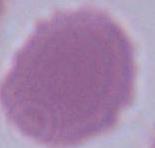
Photomicrograph. 1000x magnification. A red blood cell is seen.